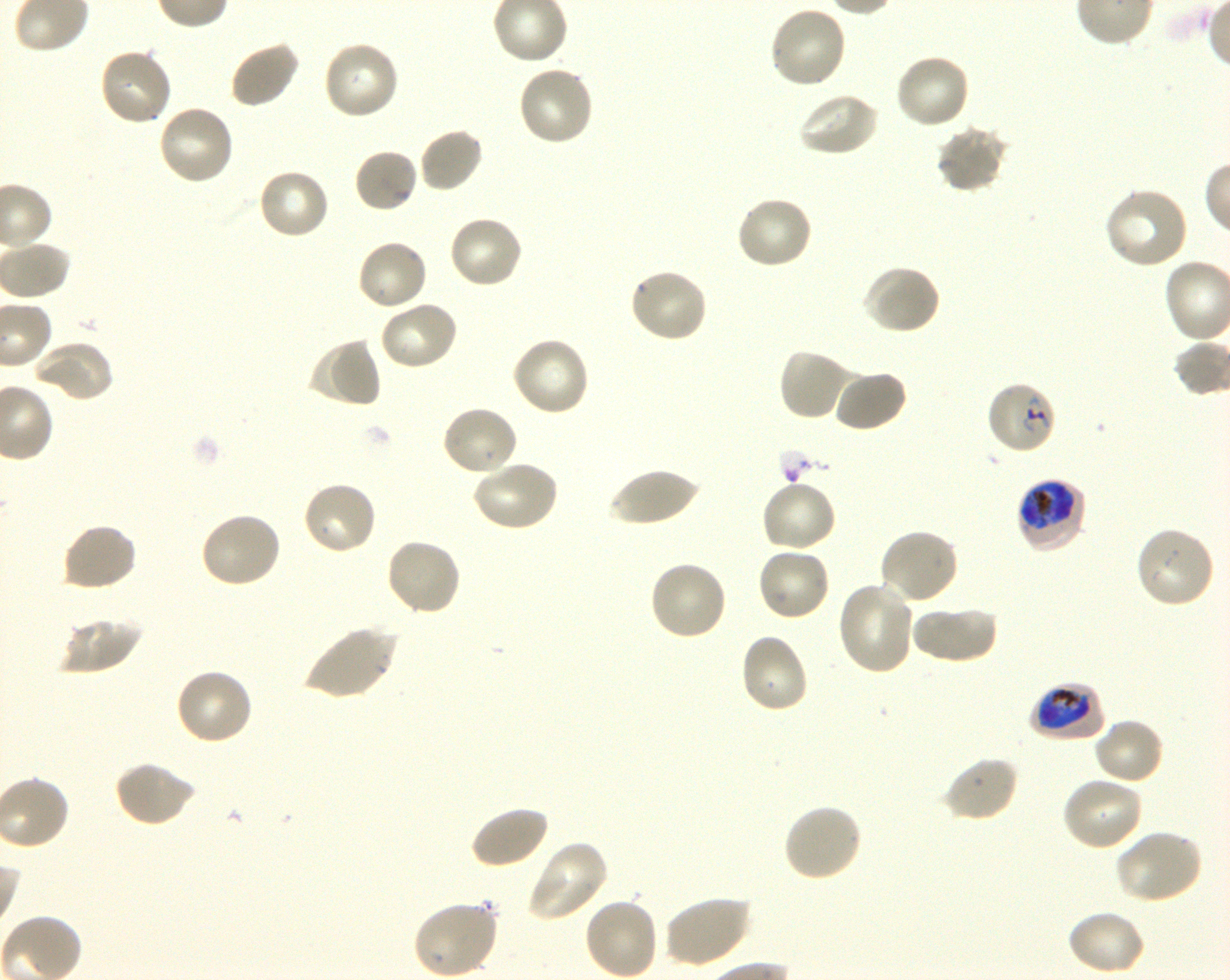
Not every red blood cell is marked. A life-cycle stage — or a range of stages, where the recorded stages span more than one — follows each staged infected red blood cell.
objective = 100x, oil immersion, numerical aperture 1.30
locations of uninfected red blood cells = approximate bounding boxes as {x1, y1, x2, y2} in pixels: {768, 5, 849, 90}, {229, 39, 301, 109}, {322, 40, 400, 121}, {97, 47, 173, 127}, {894, 53, 971, 131}, {516, 64, 594, 147}, {795, 91, 879, 158}, {156, 103, 236, 186}, {935, 126, 1009, 195}, {418, 127, 484, 195}, {353, 148, 419, 215}, {257, 167, 331, 240}, {1104, 188, 1190, 270}, {736, 194, 814, 270}, {446, 214, 524, 290}, {355, 238, 429, 312}, {861, 263, 942, 335}, {628, 268, 710, 344}, {378, 300, 459, 372}, {510, 336, 591, 418}, {307, 337, 383, 410}, {32, 340, 115, 405}, {778, 348, 856, 422}, {833, 369, 907, 433}, {441, 404, 519, 477}, {470, 459, 560, 532}, {608, 468, 699, 527}, {760, 478, 838, 553}, {301, 480, 377, 556}, {198, 511, 282, 589}, {61, 522, 139, 592}, {1133, 525, 1216, 610}, {878, 527, 960, 606}, {384, 537, 463, 618}, {756, 546, 832, 622}, {647, 561, 729, 642}, {836, 582, 916, 675}, {911, 605, 997, 664}, {56, 617, 141, 676}, {303, 625, 399, 701}, {738, 631, 809, 714}, {173, 667, 254, 746}, {1093, 717, 1165, 786}, {942, 755, 1019, 823}, {114, 759, 196, 828}, {1061, 776, 1143, 853}, {782, 803, 864, 883}, {468, 804, 549, 870}, {1115, 828, 1203, 904}, {525, 840, 609, 923}, {662, 895, 751, 968}, {584, 896, 660, 979}, {411, 899, 499, 978}, {1066, 909, 1146, 976}
locations of infected red blood cells = approximate bounding boxes as {x1, y1, x2, y2} in pixels: {986, 380, 1058, 455} ring; {1015, 477, 1088, 553} early trophozoite to early schizont; {1029, 682, 1105, 742} trophozoite
life-cycle stages observed = ring, trophozoite
stain = Giemsa
field of view = single
preparation = thin blood film
culture = P. falciparum strain 3D7, shaking, in vitro
image size = 1230×980 pixels
donor blood group = O+